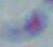
identification = Toxoplasma gondii
magnification = 1000x
modality = photomicrograph